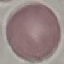
{
  "result": "no malaria parasites seen",
  "capture": "smartphone camera at the microscope eyepiece",
  "image_type": "automatically extracted cell patch, resized to 64 × 64 pixels",
  "preparation": "thin blood smear",
  "stain": "Giemsa"
}